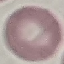

malaria_status: uninfected
stain: Giemsa
preparation: thin smear
image_type: automatically extracted cell patch, resized to 64 × 64 pixels
capture: smartphone camera at the microscope eyepiece